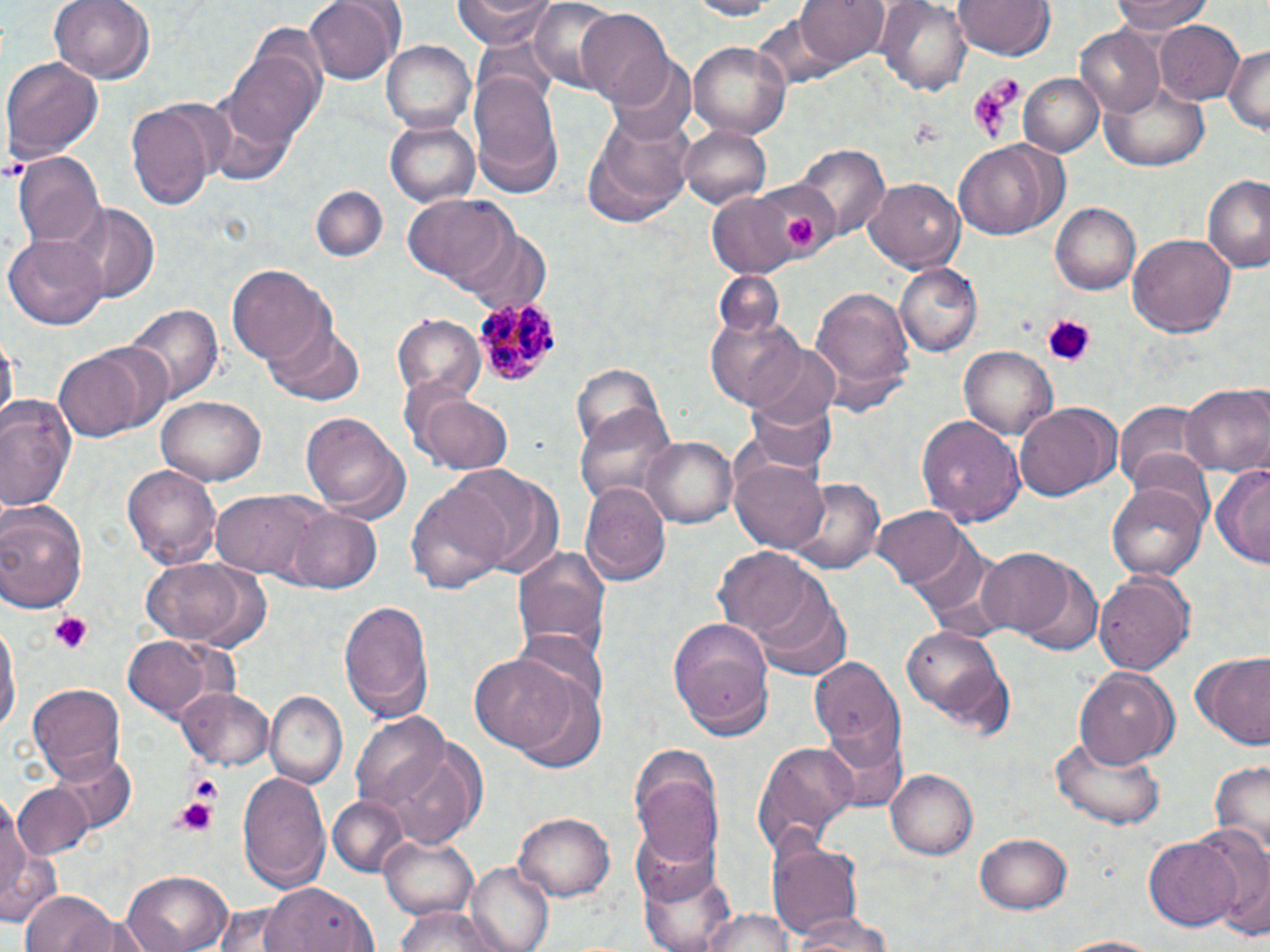

Approximate bounding boxes as (x1, y1, x2, y2) in pixels. Uninfected red blood cell locations: (49, 0, 153, 86), (307, 0, 402, 86), (453, 0, 558, 48), (527, 0, 628, 90), (684, 0, 783, 19), (798, 0, 889, 68), (954, 0, 1055, 61), (1112, 0, 1219, 32), (879, 1, 973, 93), (577, 9, 675, 108), (1153, 19, 1244, 104), (1074, 26, 1165, 117), (385, 40, 476, 132), (689, 41, 790, 139), (1222, 43, 1270, 139), (226, 49, 323, 151), (3, 57, 103, 157), (612, 61, 698, 149), (468, 71, 563, 190), (1019, 73, 1105, 159), (1102, 80, 1210, 170), (128, 97, 221, 209), (582, 114, 694, 227), (387, 120, 480, 207), (679, 124, 772, 210), (953, 141, 1067, 241), (796, 145, 888, 241), (12, 151, 105, 253), (1202, 173, 1270, 277), (865, 178, 963, 273), (309, 185, 386, 263), (707, 192, 799, 274), (404, 196, 511, 290), (1053, 201, 1141, 294), (65, 202, 158, 301), (1128, 231, 1235, 340), (3, 234, 106, 330), (896, 263, 980, 357), (228, 264, 331, 367), (807, 282, 915, 411), (127, 304, 222, 403), (705, 312, 805, 409), (391, 314, 485, 405), (263, 321, 366, 408), (3, 334, 17, 428), (745, 336, 841, 432), (960, 346, 1056, 442), (53, 347, 149, 442), (571, 361, 671, 459), (1181, 384, 1269, 476), (416, 392, 513, 474), (744, 394, 838, 478), (0, 396, 79, 513), (157, 397, 267, 484), (1117, 398, 1213, 496), (1015, 402, 1117, 500), (574, 403, 677, 513), (298, 412, 410, 519), (917, 416, 1024, 526), (644, 437, 736, 528), (730, 457, 830, 553), (122, 462, 222, 569), (452, 464, 567, 579), (1213, 466, 1269, 570), (790, 479, 885, 575), (407, 480, 510, 595), (1108, 481, 1211, 578), (581, 483, 670, 586), (210, 489, 321, 578), (0, 500, 88, 613), (871, 505, 977, 594), (282, 506, 382, 593), (513, 544, 611, 664), (714, 547, 821, 643), (973, 548, 1076, 637), (141, 562, 265, 647), (1017, 562, 1102, 654), (1094, 569, 1195, 675), (748, 588, 852, 681), (338, 599, 434, 724), (1, 613, 18, 742), (669, 618, 777, 731), (517, 623, 607, 711), (899, 625, 1007, 729), (120, 634, 229, 723), (1187, 651, 1270, 751), (807, 652, 908, 779), (471, 653, 577, 752), (1073, 666, 1179, 767), (510, 677, 609, 776), (27, 682, 126, 781), (175, 687, 273, 769), (265, 692, 347, 789), (354, 711, 451, 814), (820, 727, 906, 812), (1049, 733, 1168, 831), (751, 741, 858, 852), (380, 742, 486, 848), (626, 745, 724, 863), (43, 749, 136, 838), (1209, 762, 1270, 853), (236, 768, 331, 891), (886, 768, 977, 859), (10, 783, 94, 862), (1, 789, 35, 912), (327, 795, 412, 879), (513, 809, 615, 901), (627, 825, 722, 907), (1189, 825, 1270, 932), (975, 829, 1073, 912), (380, 834, 481, 922), (1146, 835, 1243, 933), (770, 839, 864, 942), (466, 860, 557, 952), (641, 862, 737, 952), (123, 870, 232, 952), (262, 883, 377, 950), (22, 892, 120, 952), (387, 906, 507, 952), (702, 910, 794, 952), (790, 912, 893, 951), (1048, 935, 1170, 952). Platelet locations: (968, 84, 1018, 143), (786, 216, 818, 247), (1041, 314, 1095, 364), (48, 611, 90, 651), (169, 794, 218, 842). Plasmodium malariae-infected red blood cell locations: (472, 297, 564, 388). Slide-level diagnosis: Plasmodium malariae. May-Grünwald-Giemsa stain. Captured at 1000x magnification. Image is 1270×952 pixels. Light microscopy. Thin blood smear. One field of a larger specimen.